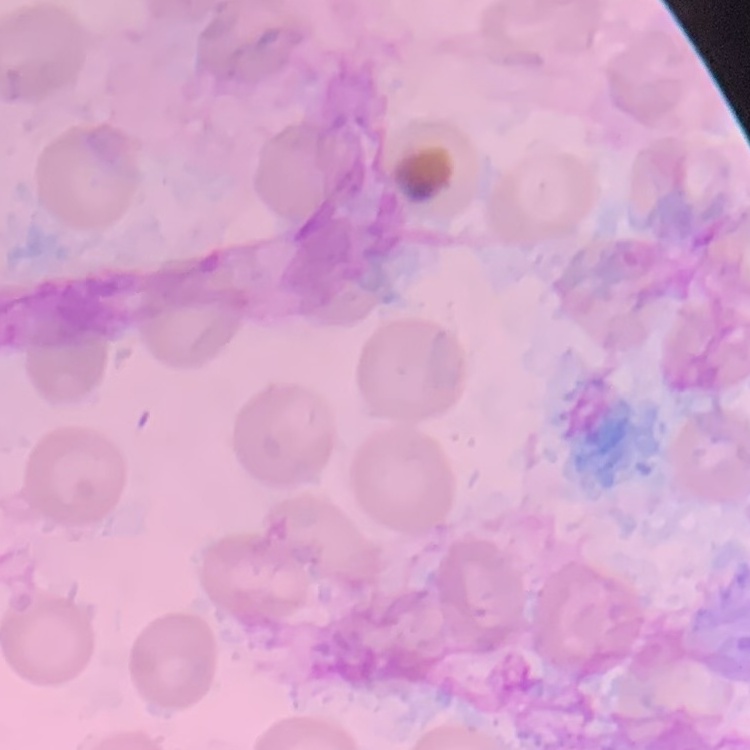

red blood cell morphology = no rouleaux formation
preparation = thin blood smear
stain = Field's or Giemsa
image type = one tile cut from a larger photomicrograph